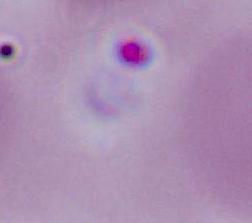

identification = Plasmodium
magnification = 400x or 1000x
modality = micrograph